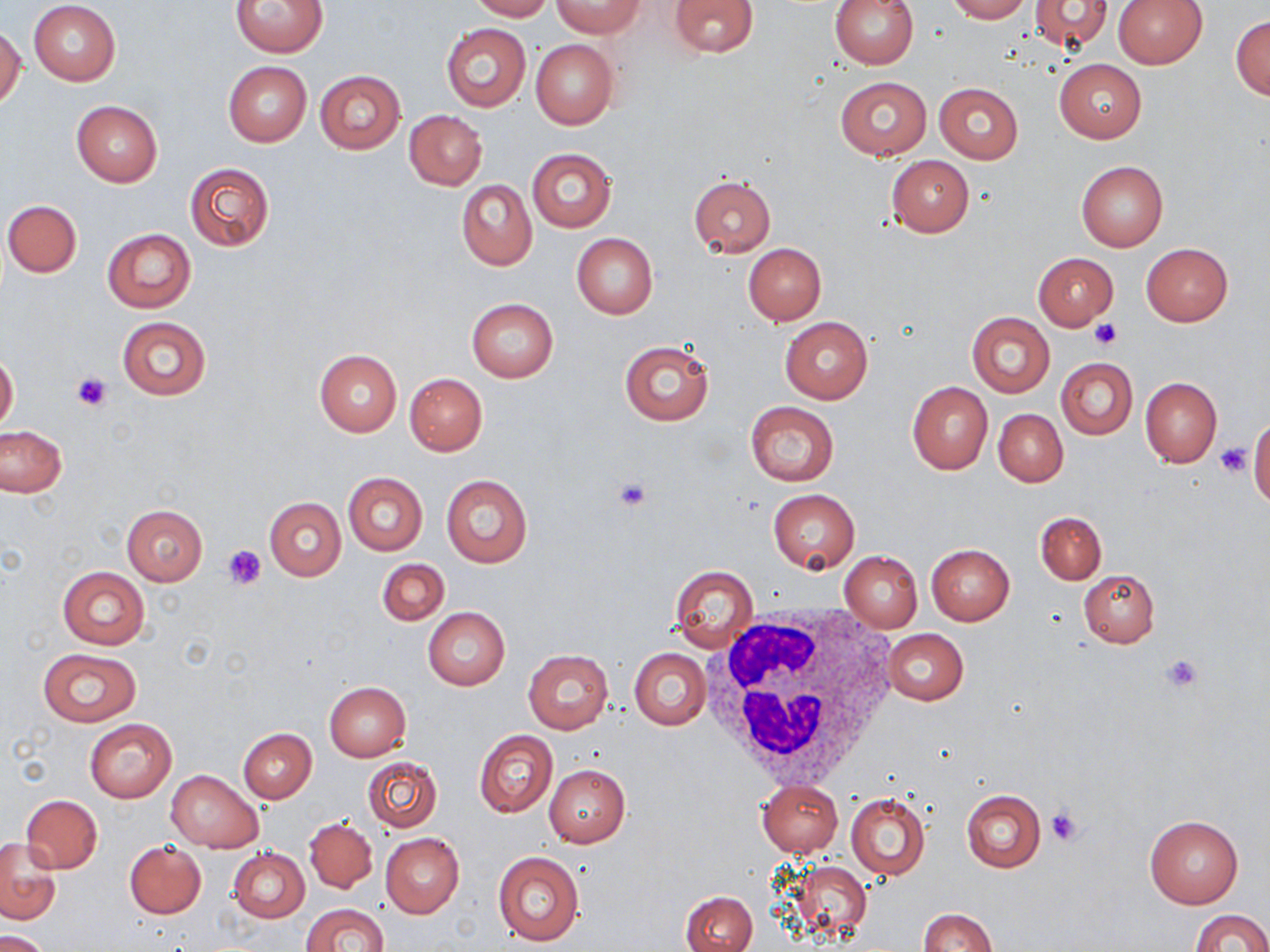 Approximate bounding boxes as [x1, y1, x2, y2] in pixels. Uninfected red blood cell locations: [28, 0, 122, 85], [231, 0, 327, 56], [469, 0, 551, 21], [667, 0, 761, 58], [830, 0, 919, 68], [945, 0, 1030, 22], [1114, 0, 1207, 67], [554, 1, 641, 37], [1027, 1, 1114, 53], [1230, 15, 1270, 99], [441, 22, 531, 113], [0, 27, 24, 110], [531, 40, 617, 129], [1054, 59, 1146, 142], [222, 61, 312, 146], [314, 70, 405, 154], [834, 76, 933, 160], [933, 82, 1024, 163], [71, 101, 162, 188], [404, 110, 487, 190], [527, 148, 617, 231], [885, 155, 974, 236], [1076, 161, 1169, 252], [184, 162, 274, 251], [688, 176, 776, 258], [457, 179, 536, 270], [3, 199, 82, 278], [102, 227, 194, 312], [571, 233, 657, 319], [742, 242, 826, 324], [1141, 243, 1233, 326], [1033, 252, 1118, 330], [465, 298, 558, 382], [967, 312, 1055, 396], [116, 315, 212, 402], [781, 317, 873, 403], [619, 342, 714, 424], [314, 349, 402, 436], [0, 353, 19, 432], [1056, 357, 1137, 439], [405, 373, 487, 455], [1139, 376, 1222, 468], [908, 381, 992, 474], [744, 400, 839, 485], [994, 409, 1067, 486], [1249, 418, 1269, 506], [0, 426, 66, 498], [342, 471, 427, 556], [440, 474, 532, 568], [767, 490, 859, 574], [265, 498, 346, 580], [121, 505, 207, 585], [1035, 511, 1107, 585], [926, 543, 1015, 625], [839, 552, 923, 631], [377, 558, 449, 625], [668, 564, 757, 652], [57, 565, 150, 650], [1079, 569, 1159, 647], [422, 607, 510, 690], [883, 628, 968, 706], [38, 648, 142, 726], [629, 648, 710, 730], [523, 649, 613, 734], [324, 682, 411, 761], [85, 717, 177, 801], [238, 728, 316, 803], [474, 730, 557, 818], [360, 757, 442, 831], [544, 764, 630, 847], [166, 770, 263, 853], [756, 779, 842, 856], [961, 790, 1045, 872], [846, 793, 929, 880], [20, 795, 102, 874], [1144, 813, 1243, 909], [304, 818, 377, 893], [380, 833, 464, 918], [1, 839, 60, 923], [124, 841, 205, 918], [229, 848, 309, 922], [493, 851, 583, 947], [788, 860, 874, 940], [680, 890, 758, 952], [302, 902, 388, 952], [917, 908, 995, 952], [1191, 910, 1269, 952], [1, 931, 51, 952]. Platelet locations: [1091, 319, 1123, 350], [70, 370, 114, 412], [1214, 443, 1251, 478], [610, 476, 654, 513], [224, 545, 267, 589], [1160, 653, 1205, 692], [1046, 803, 1088, 847]. White blood cell locations: [705, 604, 900, 790]. Slide-level diagnosis: no evidence of blood parasites. Image is 1270×952 pixels. One field of a larger specimen. 1000x magnification. Light microscopy. Thin blood smear. May-Grünwald-Giemsa-stained preparation.